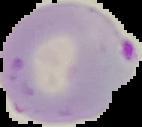
Summary:
  - Preparation: thin blood smear
  - Image size: 142×127 pixels
  - Image type: segmented cell region on a black background
  - Result: Plasmodium parasites identified